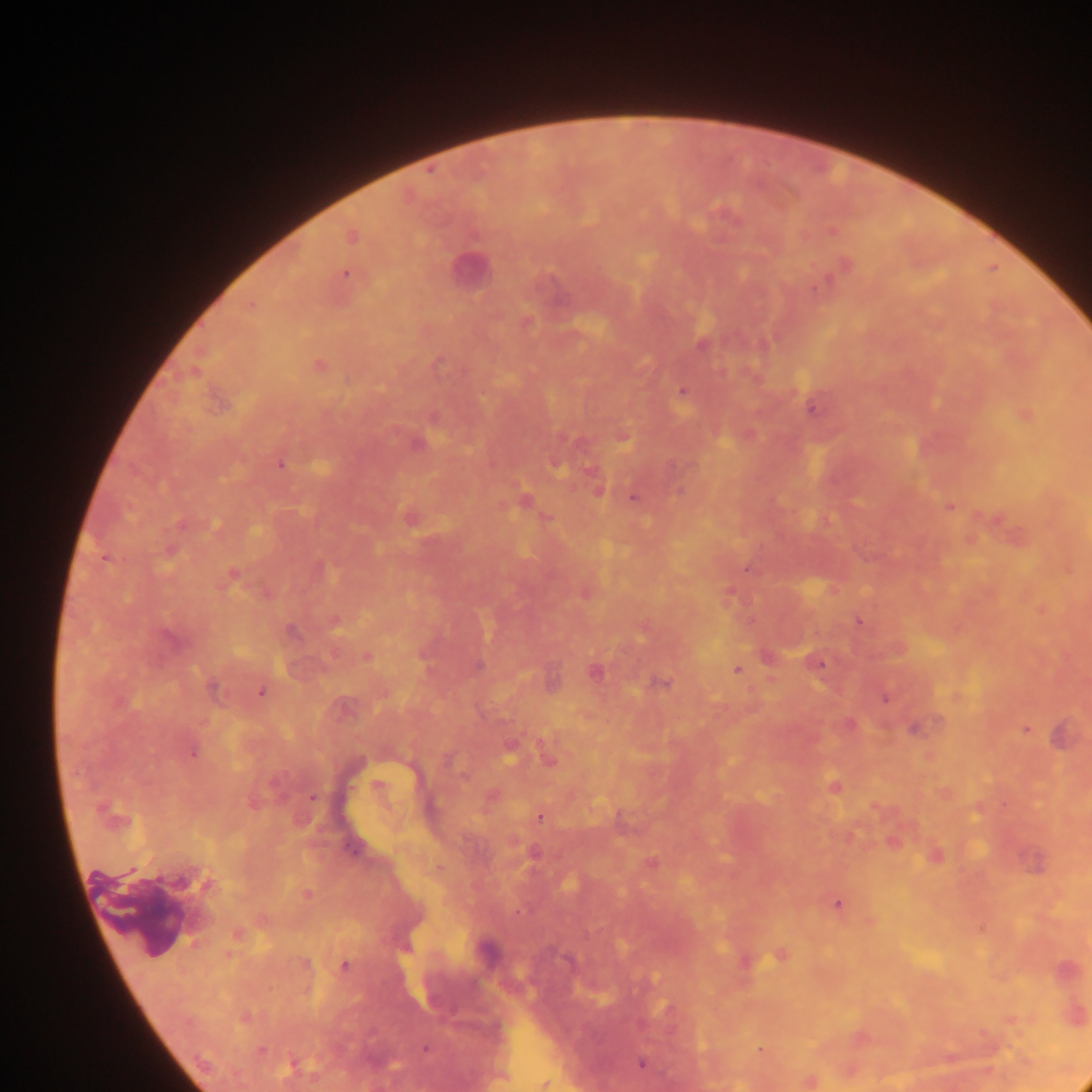

capture = mobile-phone photograph through a microscope
preparation = thick blood smear
malaria parasite locations = approximate centers as {x, y} in pixels: {725, 216}, {832, 229}, {351, 235}, {843, 265}, {345, 273}, {249, 306}, {525, 322}, {702, 343}, {317, 365}, {683, 391}, {812, 406}, {1024, 414}, {434, 418}, {748, 434}, {622, 436}, {416, 443}, {555, 462}, {280, 464}, {597, 489}, {633, 496}, {524, 501}, {949, 506}, {409, 516}, {997, 520}, {746, 568}, {231, 574}, {585, 593}, {729, 593}, {1041, 609}, {334, 620}, {859, 621}, {643, 627}, {366, 657}, {815, 662}, {478, 665}, {737, 669}, {595, 671}, {661, 682}, {215, 689}, {261, 691}, {957, 696}, {884, 697}, {915, 727}, {1025, 729}, {1061, 735}, {509, 748}, {191, 751}, {547, 756}, {377, 787}, {833, 787}, {311, 796}, {490, 796}, {875, 807}, {539, 817}, {893, 841}, {533, 853}, {935, 856}, {651, 863}, {1034, 863}, {306, 894}, {837, 904}, {237, 933}, {780, 955}, {744, 960}, {344, 966}, {245, 1017}, {1011, 1019}, {425, 1048}, {759, 1049}, {641, 1063}, {808, 1080}, {544, 1083}
country = Ghana
image size = 1092×1092 pixels
leukocyte locations = approximate centers as {x, y} in pixels: {470, 269}
field of view = single